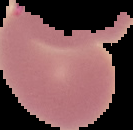
Summary:
  - Preparation: thin blood smear
  - Image size: 133×130 pixels
  - Image type: segmented cell region with the area outside set to black
  - Malaria status: uninfected